Assess the morphology of the red blood cells.
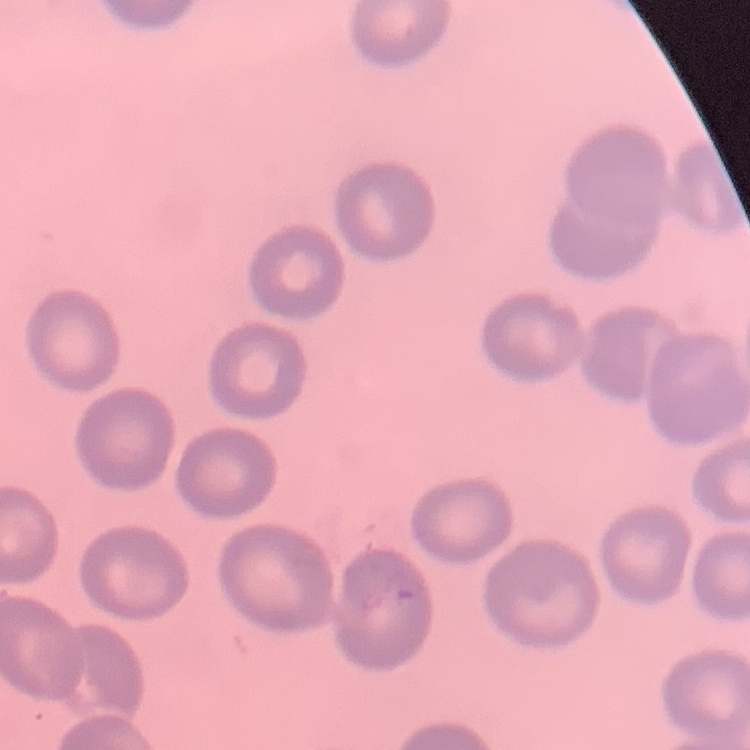
They show no rouleaux formation.

Summary:
  - Image type: square crop of a larger photomicrograph
  - Stain: Field's or Giemsa
  - Preparation: thin blood smear